Locate and identify every blood parasite.
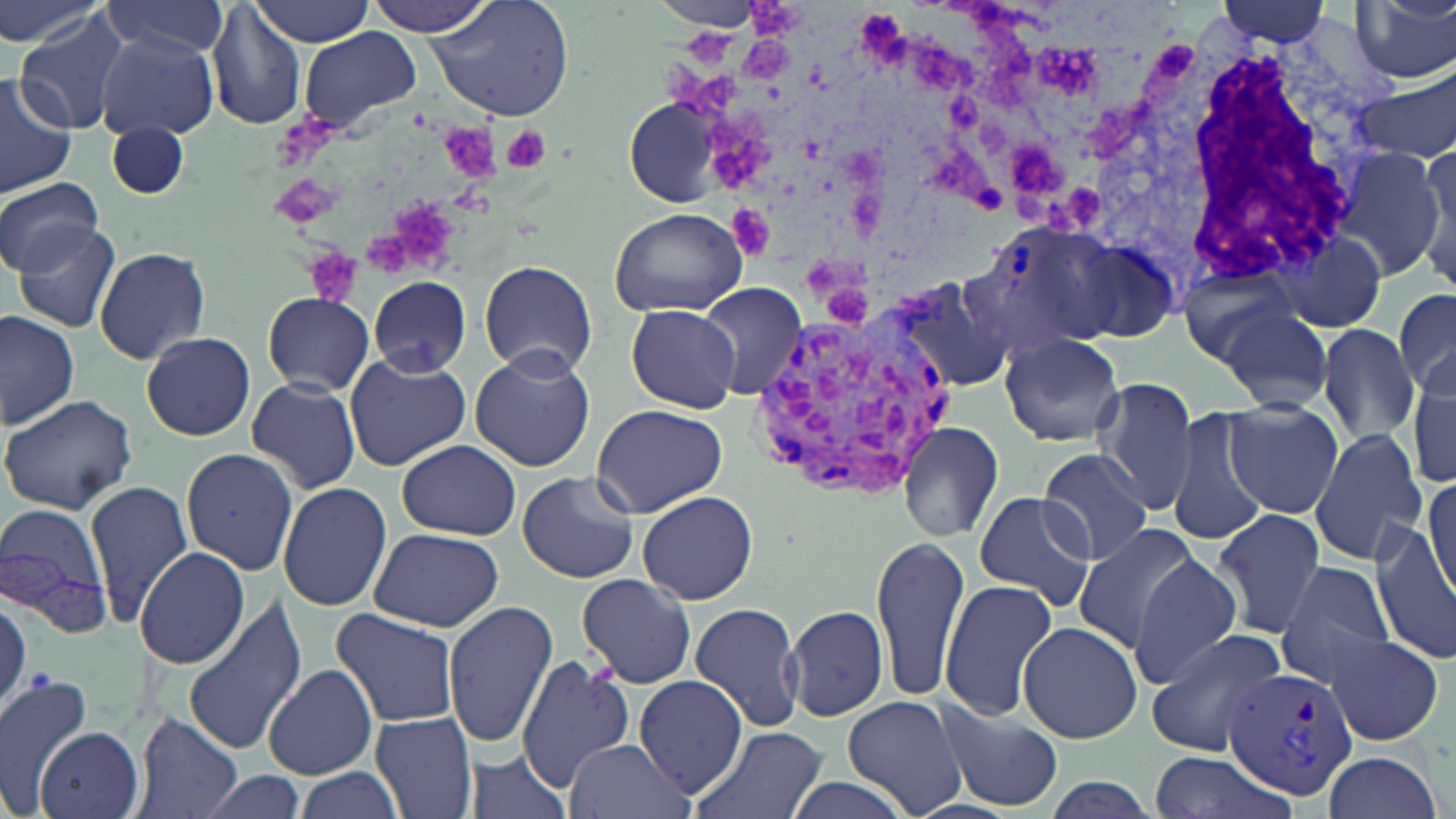

Approximate bounding boxes as named x1/y1/x2/y2 corners in pixels.
Plasmodium vivax-infected red blood cells: (x1=964, y1=218, x2=1123, y2=358), (x1=752, y1=307, x2=957, y2=498), (x1=1223, y1=664, x2=1361, y2=801).
No Plasmodium falciparum, Plasmodium ovale, Plasmodium malariae, Babesia divergens, or Trypanosoma brucei observed.

slide-level diagnosis = Plasmodium vivax
field of view = single
uninfected red blood cell locations = approximate bounding boxes as named x1/y1/x2/y2 corners in pixels: (x1=0, y1=0, x2=111, y2=52), (x1=362, y1=0, x2=497, y2=36), (x1=426, y1=0, x2=574, y2=121), (x1=651, y1=0, x2=760, y2=28), (x1=100, y1=1, x2=230, y2=61), (x1=246, y1=1, x2=376, y2=47), (x1=1208, y1=1, x2=1337, y2=49), (x1=1351, y1=2, x2=1456, y2=84), (x1=208, y1=4, x2=307, y2=129), (x1=14, y1=8, x2=139, y2=136), (x1=299, y1=28, x2=422, y2=133), (x1=95, y1=31, x2=218, y2=140), (x1=1358, y1=68, x2=1456, y2=163), (x1=0, y1=73, x2=76, y2=199), (x1=107, y1=121, x2=190, y2=200), (x1=1416, y1=141, x2=1456, y2=281), (x1=1333, y1=148, x2=1450, y2=281), (x1=0, y1=176, x2=102, y2=277), (x1=608, y1=207, x2=749, y2=317), (x1=13, y1=220, x2=124, y2=332), (x1=1053, y1=231, x2=1178, y2=342), (x1=1277, y1=234, x2=1388, y2=334), (x1=92, y1=246, x2=212, y2=364), (x1=480, y1=260, x2=598, y2=376), (x1=1177, y1=265, x2=1309, y2=373), (x1=890, y1=273, x2=1021, y2=396), (x1=369, y1=276, x2=471, y2=377), (x1=699, y1=282, x2=807, y2=402), (x1=1395, y1=285, x2=1456, y2=403), (x1=263, y1=291, x2=375, y2=394), (x1=627, y1=304, x2=740, y2=413), (x1=1219, y1=305, x2=1336, y2=415), (x1=0, y1=312, x2=79, y2=430), (x1=1314, y1=325, x2=1420, y2=446), (x1=141, y1=331, x2=256, y2=440), (x1=999, y1=334, x2=1127, y2=448), (x1=469, y1=348, x2=596, y2=472), (x1=343, y1=355, x2=472, y2=470), (x1=1408, y1=373, x2=1456, y2=491), (x1=245, y1=376, x2=362, y2=494), (x1=1091, y1=379, x2=1200, y2=513), (x1=0, y1=393, x2=139, y2=516), (x1=1222, y1=399, x2=1346, y2=520), (x1=591, y1=402, x2=730, y2=516), (x1=1168, y1=407, x2=1267, y2=544), (x1=897, y1=421, x2=1003, y2=542), (x1=1309, y1=429, x2=1431, y2=562), (x1=397, y1=440, x2=520, y2=539), (x1=181, y1=447, x2=300, y2=575), (x1=1037, y1=448, x2=1154, y2=566), (x1=1423, y1=470, x2=1456, y2=606), (x1=517, y1=471, x2=640, y2=584), (x1=84, y1=478, x2=192, y2=626), (x1=278, y1=482, x2=392, y2=612), (x1=637, y1=491, x2=758, y2=605), (x1=972, y1=492, x2=1096, y2=610), (x1=1, y1=505, x2=114, y2=634), (x1=1213, y1=507, x2=1327, y2=640), (x1=1073, y1=523, x2=1203, y2=651), (x1=1372, y1=523, x2=1456, y2=663), (x1=369, y1=527, x2=504, y2=632), (x1=872, y1=533, x2=971, y2=704), (x1=134, y1=546, x2=249, y2=668), (x1=1127, y1=555, x2=1244, y2=684), (x1=1275, y1=559, x2=1394, y2=682), (x1=577, y1=574, x2=696, y2=688), (x1=939, y1=580, x2=1059, y2=722), (x1=181, y1=596, x2=307, y2=758), (x1=442, y1=602, x2=559, y2=747), (x1=689, y1=603, x2=804, y2=733), (x1=783, y1=605, x2=889, y2=724), (x1=330, y1=607, x2=462, y2=728), (x1=1017, y1=621, x2=1142, y2=744), (x1=1144, y1=628, x2=1290, y2=756), (x1=1323, y1=632, x2=1444, y2=747), (x1=515, y1=655, x2=632, y2=792), (x1=264, y1=665, x2=377, y2=781), (x1=0, y1=674, x2=93, y2=817), (x1=633, y1=674, x2=748, y2=795), (x1=841, y1=695, x2=967, y2=818), (x1=935, y1=699, x2=1060, y2=810), (x1=369, y1=712, x2=479, y2=819), (x1=130, y1=713, x2=243, y2=819), (x1=37, y1=726, x2=143, y2=818), (x1=689, y1=726, x2=826, y2=819), (x1=563, y1=737, x2=691, y2=819), (x1=463, y1=747, x2=574, y2=819), (x1=1321, y1=750, x2=1443, y2=819), (x1=1150, y1=756, x2=1289, y2=818), (x1=292, y1=766, x2=403, y2=819), (x1=193, y1=770, x2=306, y2=819), (x1=780, y1=775, x2=915, y2=819), (x1=1040, y1=775, x2=1161, y2=819)
stain = May-Grünwald-Giemsa
white blood cell locations = approximate bounding boxes as named x1/y1/x2/y2 corners in pixels: (x1=1083, y1=13, x2=1375, y2=296)
platelet locations = approximate bounding boxes as named x1/y1/x2/y2 corners in pixels: (x1=499, y1=123, x2=549, y2=174), (x1=305, y1=248, x2=361, y2=306)
modality = light microscopy
preparation = thin blood smear
magnification = 1000x
image size = 1456×819 pixels